Locate and identify every blood parasite.
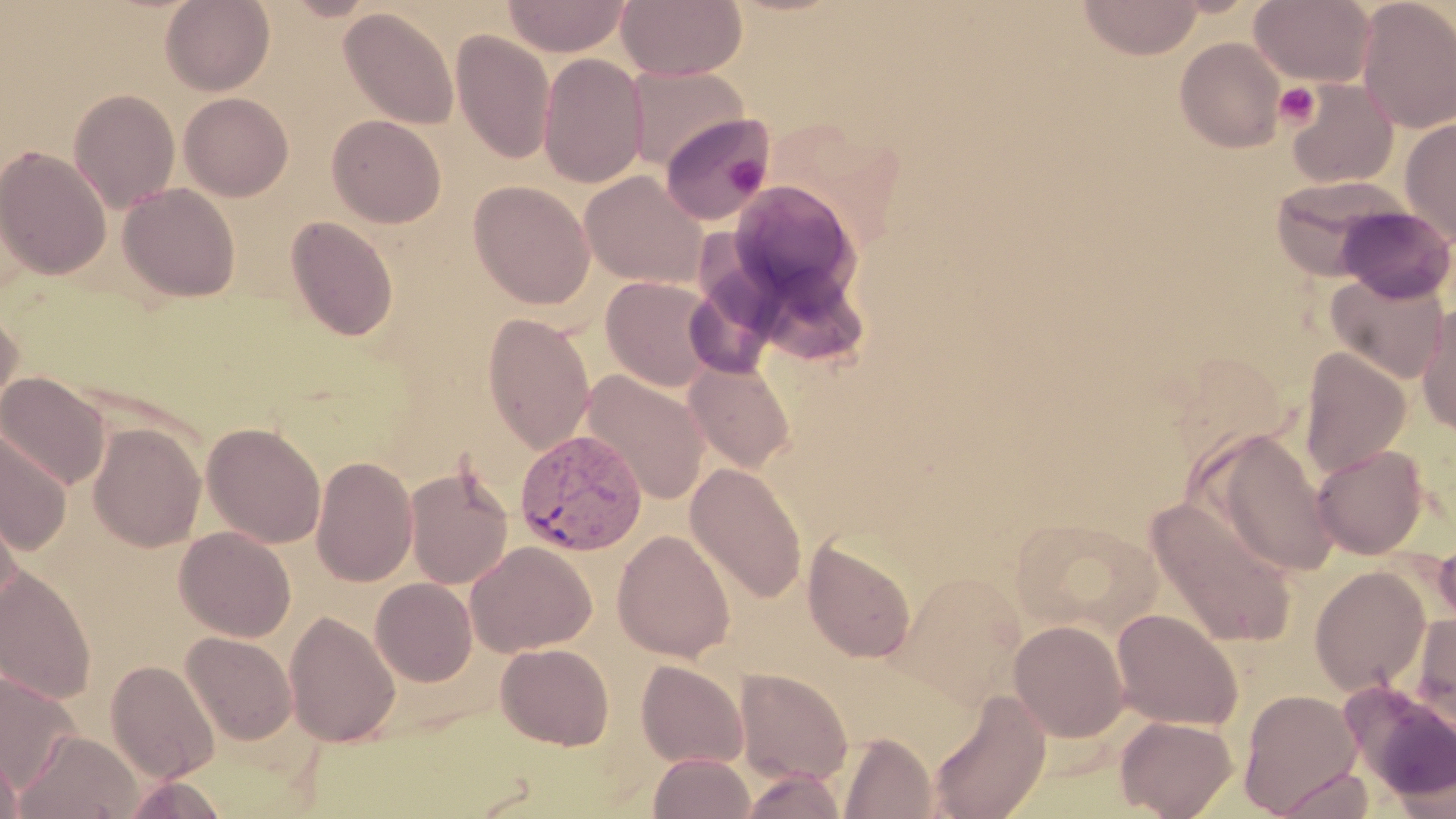

Approximate bounding boxes as [x1, y1, x2, y2] in pixels.
Plasmodium vivax-infected red blood cells: [514, 429, 648, 556].
No Plasmodium falciparum, Plasmodium ovale, Plasmodium malariae, Babesia divergens, or Trypanosoma brucei observed.

slide_level_diagnosis: Plasmodium vivax
platelet_locations: 'approximate bounding boxes as [x1, y1, x2, y2] in pixels: [1275, 82, 1320, 129], [724, 154, 768, 194]'
modality: optical microscopy
magnification: 1000x
field_of_view: single
preparation: thin blood film
image_size: 1456×819 pixels
uninfected_red_blood_cell_locations: 'approximate bounding boxes as [x1, y1, x2, y2] in pixels: [160, 0, 274, 96], [502, 0, 631, 57], [617, 0, 747, 82], [1077, 0, 1205, 60], [1250, 0, 1376, 86], [1356, 0, 1456, 134], [339, 8, 459, 128], [451, 31, 555, 165], [1174, 37, 1286, 153], [537, 53, 649, 189], [625, 65, 749, 171], [1285, 78, 1399, 190], [68, 89, 180, 213], [179, 92, 293, 201], [659, 113, 771, 224], [327, 115, 447, 227], [1399, 117, 1456, 248], [0, 146, 112, 280], [580, 170, 709, 288], [1269, 175, 1411, 281], [469, 180, 595, 309], [727, 181, 860, 309], [118, 183, 241, 302], [1335, 206, 1455, 303], [285, 216, 400, 341], [1326, 270, 1450, 383], [600, 275, 720, 391], [0, 303, 24, 428], [1417, 304, 1456, 438], [482, 311, 595, 454], [1298, 347, 1411, 480], [685, 361, 795, 472], [1, 370, 110, 491], [582, 370, 709, 506], [202, 422, 326, 547], [88, 424, 205, 551], [0, 430, 72, 552], [1205, 430, 1339, 577], [1312, 445, 1428, 559], [311, 455, 418, 587], [405, 463, 514, 590], [686, 463, 807, 604], [0, 485, 25, 610], [1146, 496, 1298, 648], [1011, 517, 1162, 639], [174, 526, 296, 642], [612, 530, 736, 662], [1430, 536, 1456, 636], [803, 538, 916, 663], [465, 541, 596, 657], [1308, 565, 1431, 696], [0, 566, 96, 703], [894, 569, 1027, 707], [370, 578, 478, 687], [1110, 608, 1244, 731], [284, 611, 400, 747], [1411, 614, 1456, 736], [1009, 620, 1129, 742], [181, 632, 297, 745], [496, 643, 614, 750], [636, 659, 749, 769], [106, 660, 219, 783], [0, 669, 82, 796], [733, 669, 852, 786], [1238, 688, 1362, 816], [927, 691, 1051, 819], [1115, 715, 1238, 818], [14, 730, 142, 819], [838, 732, 937, 819], [0, 743, 23, 819], [648, 752, 756, 819], [1272, 767, 1377, 819], [740, 768, 847, 818], [121, 773, 230, 818]'
stain: May-Grünwald-Giemsa